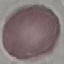 Result: negative for malaria parasites. Cell patch, automatically extracted from a larger field of view and resized to 64 × 64 pixels. Giemsa stain. Acquired by smartphone through the microscope eyepiece. Thin blood film.